Classify this cell by malaria status.
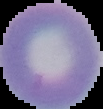

Uninfected.

preparation = thin blood film
image size = 103×109 pixels
image type = segmented cell region with the area outside set to black